Outline each Plasmodium ovale-infected red blood cell.
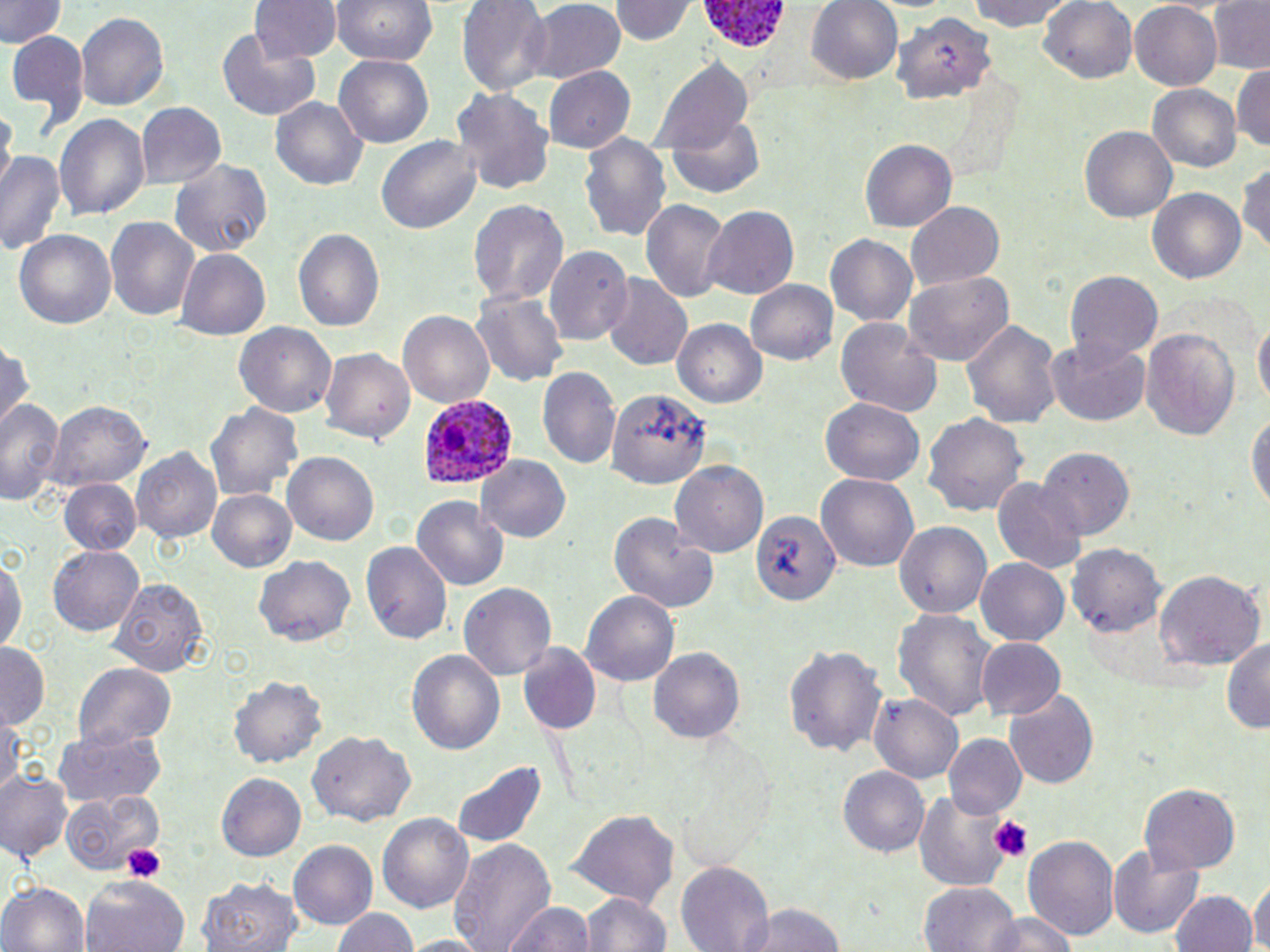

Approximate bounding boxes as [x1, y1, x2, y2] in pixels.
Plasmodium ovale-infected red blood cells: [698, 0, 795, 60], [419, 394, 517, 487].

Summary:
  - Uninfected red blood cell locations: [0, 0, 64, 49], [251, 0, 340, 62], [330, 0, 439, 64], [455, 0, 552, 95], [614, 0, 694, 45], [805, 0, 905, 85], [963, 0, 1079, 33], [1038, 0, 1136, 86], [1206, 0, 1270, 73], [521, 2, 627, 83], [1128, 5, 1222, 89], [76, 12, 168, 113], [894, 13, 996, 107], [6, 30, 88, 131], [217, 33, 320, 121], [335, 55, 434, 149], [654, 57, 755, 155], [1232, 61, 1270, 154], [544, 68, 635, 152], [1149, 84, 1242, 174], [452, 86, 554, 199], [271, 97, 368, 190], [135, 101, 226, 189], [2, 105, 15, 190], [55, 111, 151, 225], [667, 118, 766, 200], [1077, 126, 1176, 223], [578, 133, 672, 245], [376, 134, 484, 235], [861, 138, 957, 229], [0, 149, 67, 255], [170, 160, 270, 258], [1238, 162, 1270, 257], [1147, 185, 1247, 284], [467, 198, 568, 309], [641, 198, 729, 303], [907, 202, 1005, 289], [702, 204, 800, 301], [106, 220, 197, 321], [13, 229, 119, 330], [294, 229, 385, 337], [826, 234, 918, 326], [548, 246, 634, 345], [176, 249, 274, 340], [1063, 268, 1166, 366], [903, 269, 1016, 364], [601, 275, 692, 370], [745, 279, 839, 367], [472, 291, 567, 388], [399, 308, 496, 409], [1253, 314, 1269, 414], [835, 316, 944, 419], [961, 316, 1062, 432], [673, 320, 768, 409], [234, 322, 337, 419], [1142, 325, 1242, 442], [1044, 338, 1152, 428], [0, 343, 31, 430], [320, 351, 415, 444], [538, 366, 621, 474], [610, 390, 710, 491], [0, 397, 65, 505], [820, 398, 925, 486], [44, 399, 154, 489], [205, 400, 305, 506], [1247, 405, 1270, 519], [922, 413, 1028, 518], [133, 447, 223, 547], [1040, 448, 1132, 541], [283, 452, 380, 546], [478, 455, 574, 543], [671, 461, 769, 557], [816, 470, 918, 570], [992, 471, 1087, 573], [59, 480, 143, 556], [207, 487, 299, 573], [412, 493, 509, 592], [610, 510, 717, 614], [752, 511, 839, 605], [896, 522, 992, 620], [360, 542, 449, 645], [1068, 545, 1165, 636], [47, 546, 143, 636], [0, 554, 27, 656], [256, 555, 356, 645], [975, 557, 1070, 646], [1154, 569, 1264, 670], [110, 574, 210, 677], [456, 582, 558, 682], [581, 588, 678, 687], [894, 609, 998, 726], [1221, 636, 1270, 734], [976, 638, 1066, 721], [0, 642, 50, 730], [521, 643, 599, 735], [786, 645, 887, 760], [647, 646, 745, 746], [407, 647, 507, 759], [71, 662, 179, 748], [231, 672, 326, 767], [1004, 690, 1101, 791], [870, 694, 965, 784], [0, 715, 25, 793], [52, 725, 168, 808], [310, 729, 415, 826], [944, 734, 1026, 816], [450, 757, 550, 852], [838, 767, 929, 857], [0, 771, 74, 865], [217, 772, 306, 860], [1138, 785, 1240, 872], [911, 788, 1018, 891], [63, 791, 168, 875], [569, 809, 679, 909], [377, 812, 475, 915], [1024, 834, 1118, 939], [449, 838, 555, 952], [289, 841, 378, 929], [1107, 847, 1205, 940], [676, 862, 774, 952], [195, 875, 299, 952], [83, 876, 186, 952], [1252, 877, 1268, 952], [0, 880, 89, 952], [917, 882, 1019, 952], [577, 890, 673, 952], [1172, 890, 1257, 952], [501, 899, 597, 952], [740, 900, 847, 952], [330, 905, 420, 952], [978, 913, 1083, 952], [398, 934, 489, 952]
  - Platelet locations: [988, 814, 1034, 859], [123, 841, 166, 881]
  - Slide-level diagnosis: Plasmodium ovale
  - Magnification: 1000x
  - Image size: 1270×952 pixels
  - Preparation: thin blood smear
  - Stain: May-Grünwald-Giemsa
  - Modality: optical microscopy
  - Field of view: one of a larger specimen